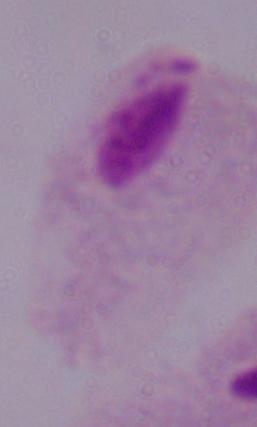

modality = micrograph
identification = trichomonad
magnification = 1000x